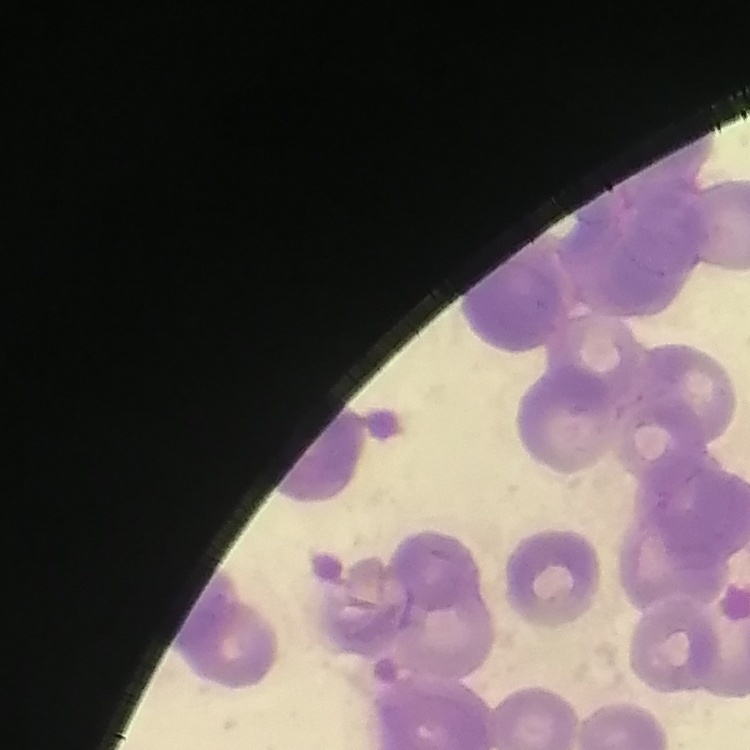
The erythrocytes show rouleaux formation. Square crop of a larger photomicrograph. Field's or Giemsa stain. Thin blood smear.